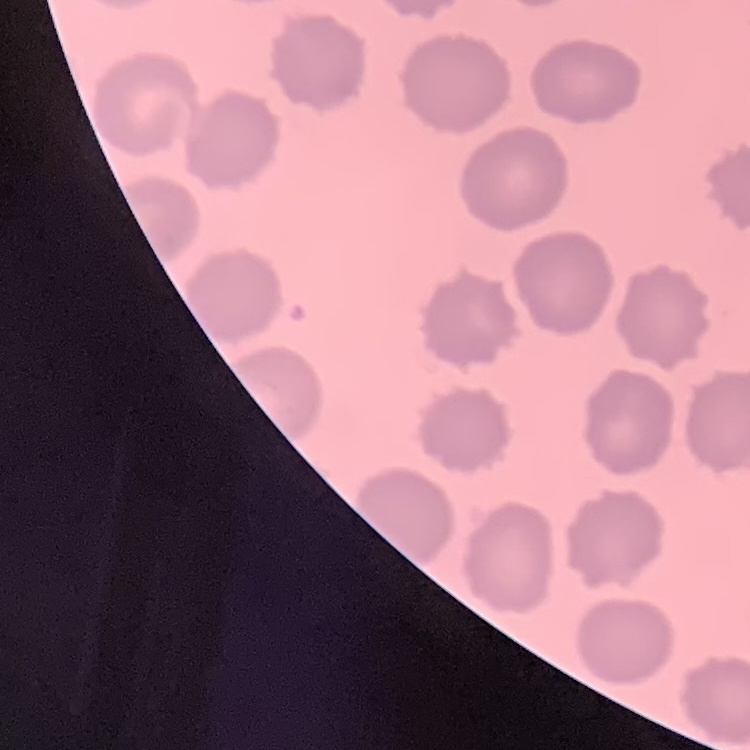

Summary:
  - Erythrocyte morphology: no rouleaux formation
  - Preparation: thin blood film
  - Stain: Field's or Giemsa
  - Image type: square crop of a larger photomicrograph